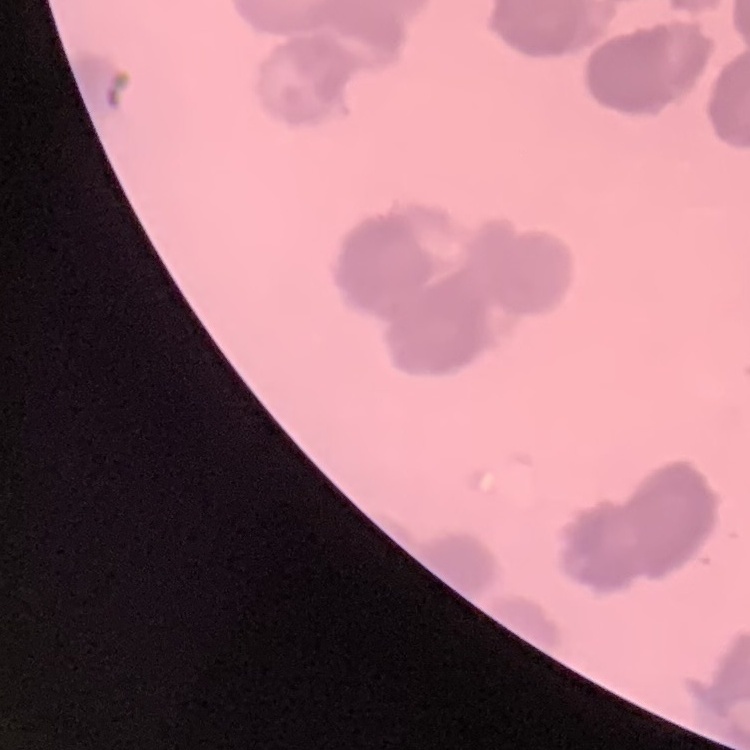 The red blood cells exhibit rouleaux formation. Field's or Giemsa stain. Square crop of a larger photomicrograph. Thin peripheral smear.